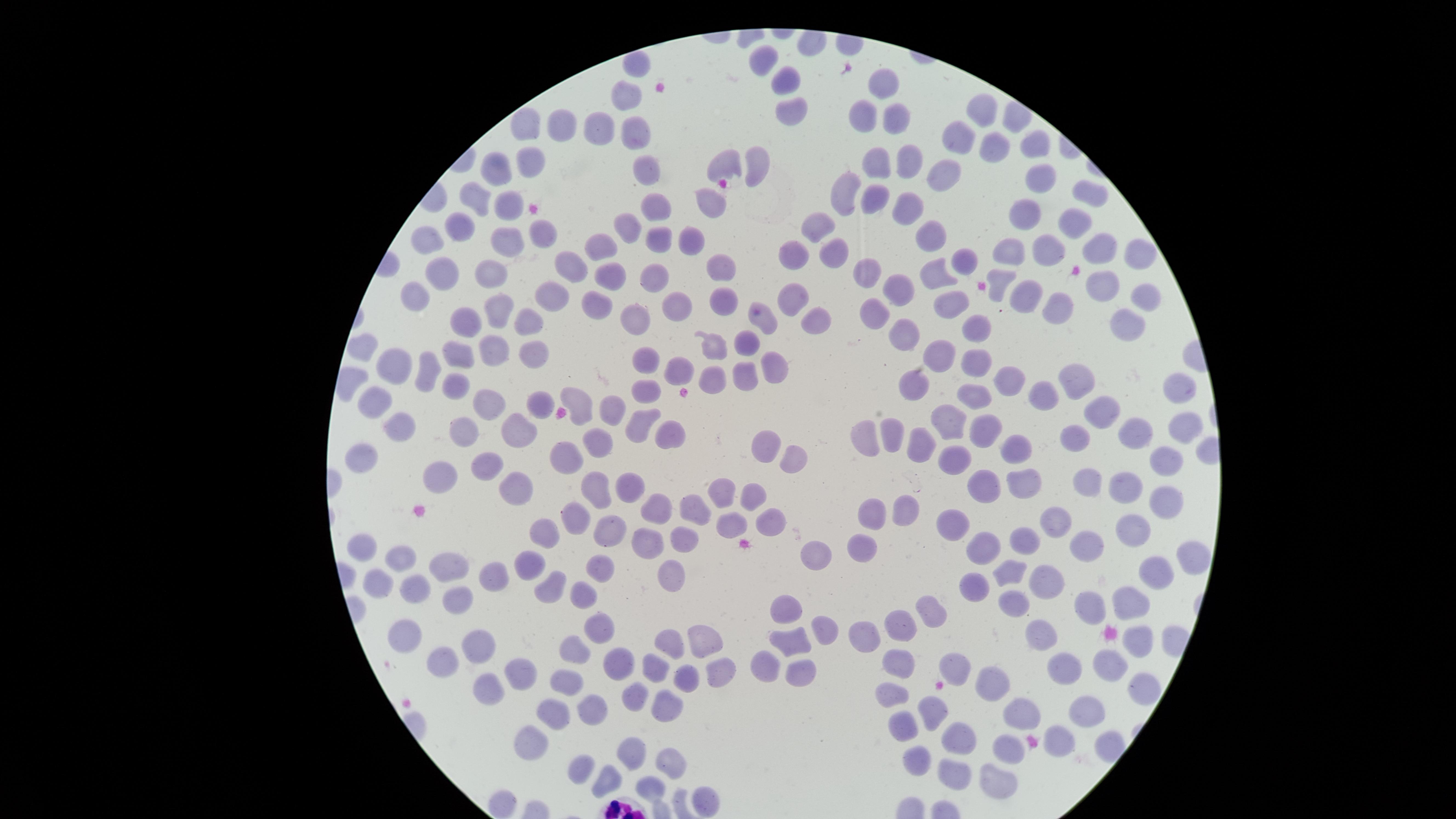
presence = no malaria parasites identified
visible region = circular
preparation = thin blood film
field of view = single
stain = Giemsa
image size = 1456×819 pixels
uninfected RBCs = approximate marker points, in pixels from the top-left corner: (x=768, y=59), (x=637, y=67), (x=887, y=80), (x=787, y=82), (x=626, y=98), (x=792, y=110), (x=983, y=113), (x=534, y=119), (x=867, y=119), (x=899, y=120), (x=604, y=126), (x=636, y=130), (x=564, y=131), (x=965, y=138), (x=1034, y=147), (x=996, y=152), (x=530, y=159), (x=759, y=162), (x=910, y=162), (x=731, y=163), (x=646, y=165), (x=881, y=165), (x=502, y=167), (x=949, y=170), (x=1045, y=181), (x=848, y=193), (x=1089, y=195), (x=874, y=197), (x=711, y=201), (x=481, y=204), (x=656, y=205), (x=909, y=206), (x=508, y=207), (x=1025, y=221), (x=1075, y=222), (x=818, y=224), (x=628, y=228), (x=543, y=229), (x=462, y=230), (x=929, y=236), (x=694, y=238), (x=431, y=240), (x=662, y=240), (x=509, y=242), (x=605, y=249), (x=791, y=250), (x=1050, y=251), (x=1098, y=251), (x=1011, y=253), (x=834, y=255), (x=1137, y=256), (x=962, y=263), (x=573, y=264), (x=718, y=265), (x=445, y=272), (x=612, y=272), (x=491, y=273), (x=866, y=273), (x=937, y=276), (x=654, y=277), (x=998, y=285), (x=1102, y=285), (x=897, y=290), (x=1143, y=293), (x=419, y=294), (x=554, y=295), (x=1027, y=296), (x=799, y=298), (x=949, y=299), (x=726, y=301), (x=1065, y=302), (x=600, y=303), (x=675, y=304), (x=502, y=307), (x=877, y=310), (x=765, y=316), (x=634, y=318), (x=527, y=321), (x=463, y=322), (x=816, y=322), (x=977, y=327), (x=1129, y=328), (x=905, y=336), (x=748, y=343), (x=716, y=348), (x=940, y=351), (x=363, y=352), (x=462, y=355), (x=534, y=355), (x=498, y=356), (x=645, y=361), (x=974, y=361), (x=402, y=363), (x=774, y=365), (x=431, y=368), (x=682, y=368), (x=1079, y=376), (x=746, y=379), (x=1014, y=381), (x=715, y=382), (x=460, y=384), (x=912, y=388), (x=1183, y=389), (x=650, y=392), (x=1048, y=393), (x=979, y=395), (x=376, y=402), (x=581, y=402), (x=495, y=404), (x=544, y=405), (x=1099, y=408), (x=611, y=411), (x=644, y=419), (x=953, y=422), (x=392, y=424), (x=520, y=428), (x=985, y=428), (x=1185, y=429), (x=466, y=433), (x=868, y=435), (x=1138, y=435), (x=668, y=436), (x=894, y=436), (x=775, y=437), (x=1074, y=437), (x=602, y=439), (x=925, y=444), (x=1018, y=448), (x=359, y=453), (x=955, y=455), (x=570, y=456), (x=791, y=457), (x=1168, y=460), (x=493, y=461), (x=441, y=473), (x=1091, y=482), (x=517, y=483), (x=1022, y=483), (x=1127, y=483), (x=630, y=485), (x=725, y=488), (x=600, y=489), (x=988, y=490), (x=753, y=499), (x=1169, y=501), (x=698, y=505), (x=659, y=507), (x=875, y=511), (x=909, y=511), (x=580, y=517), (x=772, y=522), (x=1059, y=522), (x=728, y=527), (x=1138, y=527), (x=954, y=528), (x=549, y=532), (x=613, y=532), (x=1027, y=536), (x=649, y=537), (x=683, y=537), (x=1089, y=542), (x=982, y=547), (x=861, y=548), (x=363, y=550), (x=821, y=558), (x=400, y=561), (x=1192, y=563), (x=532, y=565), (x=602, y=566), (x=445, y=567), (x=1013, y=571), (x=674, y=573), (x=1151, y=573), (x=495, y=576), (x=973, y=584), (x=1046, y=585), (x=551, y=586), (x=419, y=587), (x=380, y=588), (x=582, y=596), (x=1012, y=597), (x=1130, y=601), (x=456, y=602), (x=1092, y=606), (x=787, y=610), (x=934, y=611), (x=600, y=625), (x=904, y=628), (x=405, y=630), (x=823, y=632), (x=711, y=635), (x=672, y=637), (x=865, y=640), (x=1046, y=640), (x=1137, y=640), (x=478, y=642), (x=793, y=642), (x=576, y=647), (x=446, y=659), (x=955, y=659), (x=623, y=663), (x=775, y=664), (x=900, y=664), (x=1112, y=664), (x=663, y=665), (x=1071, y=667), (x=517, y=669), (x=718, y=671), (x=804, y=674), (x=681, y=676), (x=993, y=676), (x=567, y=680), (x=1142, y=687), (x=490, y=688), (x=891, y=694), (x=633, y=700), (x=592, y=703), (x=667, y=708), (x=932, y=708), (x=1023, y=710), (x=1082, y=710), (x=556, y=712), (x=903, y=720), (x=529, y=736), (x=960, y=736), (x=1059, y=742), (x=1006, y=748), (x=628, y=753), (x=671, y=755), (x=581, y=757), (x=916, y=762), (x=605, y=774), (x=953, y=774), (x=1007, y=777), (x=652, y=786), (x=705, y=794), (x=505, y=801)
capture = smartphone photograph through the microscope eyepiece